Identify the parasite.
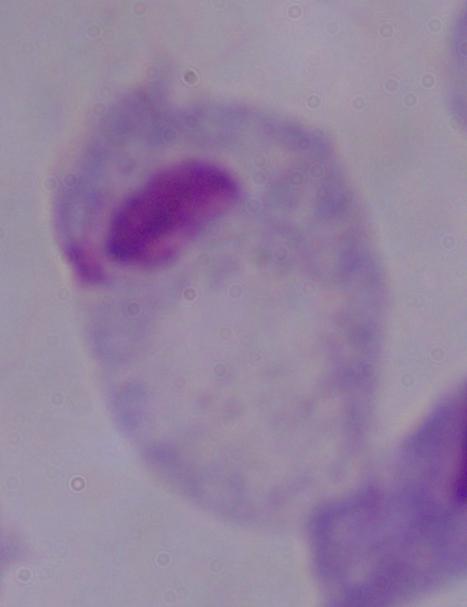
This is a trichomonad.

1000x magnification. Photomicrograph.